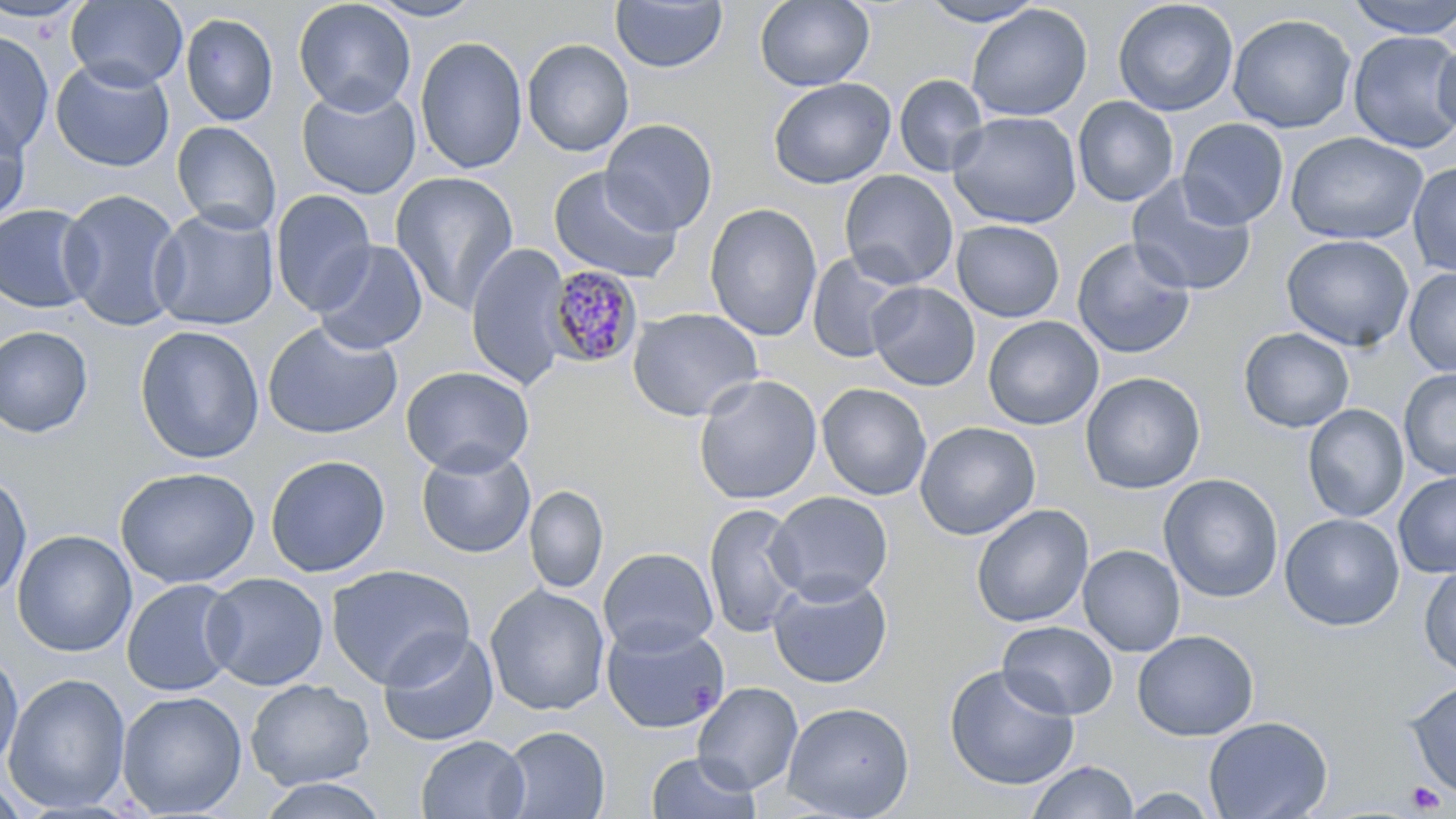
slide_level_diagnosis: Plasmodium malariae
preparation: thin blood film
modality: optical microscopy
plasmodium_malariae_infected_red_blood_cell_locations: 'approximate bounding boxes as named x1/y1/x2/y2 corners in pixels: (x1=545, y1=266, x2=643, y2=368)'
platelet_locations: 'approximate bounding boxes as named x1/y1/x2/y2 corners in pixels: (x1=1406, y1=781, x2=1444, y2=814)'
stain: May-Grünwald-Giemsa
uninfected_red_blood_cell_locations: 'approximate bounding boxes as named x1/y1/x2/y2 corners in pixels: (x1=66, y1=0, x2=188, y2=91), (x1=293, y1=0, x2=417, y2=115), (x1=364, y1=0, x2=484, y2=22), (x1=609, y1=0, x2=728, y2=73), (x1=755, y1=0, x2=874, y2=91), (x1=917, y1=0, x2=1046, y2=27), (x1=1112, y1=0, x2=1238, y2=116), (x1=1344, y1=0, x2=1456, y2=39), (x1=0, y1=1, x2=92, y2=23), (x1=966, y1=4, x2=1092, y2=122), (x1=180, y1=12, x2=279, y2=126), (x1=1227, y1=14, x2=1357, y2=134), (x1=0, y1=30, x2=55, y2=155), (x1=1348, y1=30, x2=1456, y2=153), (x1=415, y1=36, x2=528, y2=174), (x1=521, y1=38, x2=635, y2=157), (x1=1432, y1=38, x2=1456, y2=139), (x1=50, y1=58, x2=175, y2=172), (x1=894, y1=74, x2=989, y2=176), (x1=767, y1=77, x2=897, y2=189), (x1=296, y1=84, x2=421, y2=199), (x1=1072, y1=96, x2=1179, y2=206), (x1=0, y1=104, x2=32, y2=228), (x1=947, y1=111, x2=1082, y2=229), (x1=601, y1=118, x2=718, y2=235), (x1=1177, y1=118, x2=1289, y2=229), (x1=171, y1=121, x2=282, y2=235), (x1=1286, y1=132, x2=1428, y2=245), (x1=1408, y1=162, x2=1456, y2=277), (x1=548, y1=166, x2=683, y2=284), (x1=839, y1=170, x2=959, y2=289), (x1=390, y1=172, x2=519, y2=315), (x1=1126, y1=175, x2=1257, y2=296), (x1=58, y1=188, x2=185, y2=331), (x1=270, y1=189, x2=377, y2=315), (x1=704, y1=203, x2=823, y2=342), (x1=0, y1=204, x2=97, y2=314), (x1=149, y1=207, x2=279, y2=330), (x1=951, y1=220, x2=1065, y2=322), (x1=1281, y1=234, x2=1414, y2=352), (x1=1071, y1=237, x2=1196, y2=360), (x1=312, y1=239, x2=428, y2=355), (x1=466, y1=243, x2=573, y2=390), (x1=806, y1=252, x2=913, y2=363), (x1=1404, y1=267, x2=1456, y2=377), (x1=867, y1=282, x2=980, y2=391), (x1=627, y1=307, x2=764, y2=422), (x1=983, y1=316, x2=1103, y2=430), (x1=261, y1=321, x2=404, y2=439), (x1=0, y1=325, x2=94, y2=438), (x1=134, y1=325, x2=265, y2=464), (x1=1239, y1=328, x2=1354, y2=432), (x1=400, y1=365, x2=534, y2=476), (x1=1399, y1=369, x2=1456, y2=481), (x1=1080, y1=371, x2=1206, y2=495), (x1=693, y1=374, x2=822, y2=506), (x1=817, y1=382, x2=932, y2=500), (x1=1303, y1=404, x2=1409, y2=523), (x1=915, y1=421, x2=1040, y2=540), (x1=416, y1=445, x2=535, y2=558), (x1=265, y1=454, x2=390, y2=578), (x1=115, y1=466, x2=259, y2=589), (x1=1393, y1=472, x2=1456, y2=578), (x1=0, y1=473, x2=33, y2=601), (x1=1158, y1=473, x2=1284, y2=603), (x1=525, y1=485, x2=608, y2=593), (x1=767, y1=491, x2=893, y2=604), (x1=703, y1=502, x2=805, y2=639), (x1=971, y1=504, x2=1094, y2=628), (x1=1280, y1=513, x2=1404, y2=631), (x1=12, y1=529, x2=137, y2=657), (x1=1078, y1=544, x2=1185, y2=657), (x1=598, y1=547, x2=718, y2=656), (x1=326, y1=564, x2=475, y2=688), (x1=1418, y1=566, x2=1456, y2=678), (x1=202, y1=572, x2=329, y2=691), (x1=768, y1=574, x2=893, y2=689), (x1=121, y1=578, x2=241, y2=697), (x1=485, y1=585, x2=610, y2=716), (x1=998, y1=620, x2=1118, y2=720), (x1=601, y1=621, x2=729, y2=733), (x1=378, y1=629, x2=499, y2=747), (x1=1132, y1=630, x2=1260, y2=741), (x1=0, y1=651, x2=23, y2=773), (x1=943, y1=664, x2=1079, y2=791), (x1=3, y1=673, x2=132, y2=814), (x1=246, y1=678, x2=375, y2=791), (x1=1405, y1=680, x2=1456, y2=800), (x1=692, y1=682, x2=803, y2=794), (x1=116, y1=690, x2=247, y2=817), (x1=781, y1=701, x2=915, y2=819), (x1=1203, y1=715, x2=1333, y2=819), (x1=499, y1=726, x2=610, y2=819), (x1=415, y1=735, x2=530, y2=819), (x1=645, y1=751, x2=762, y2=819), (x1=1027, y1=760, x2=1138, y2=819), (x1=0, y1=776, x2=30, y2=819), (x1=256, y1=777, x2=390, y2=819), (x1=1118, y1=788, x2=1223, y2=818)'
magnification: 1000x
image_size: 1456×819 pixels
field_of_view: single